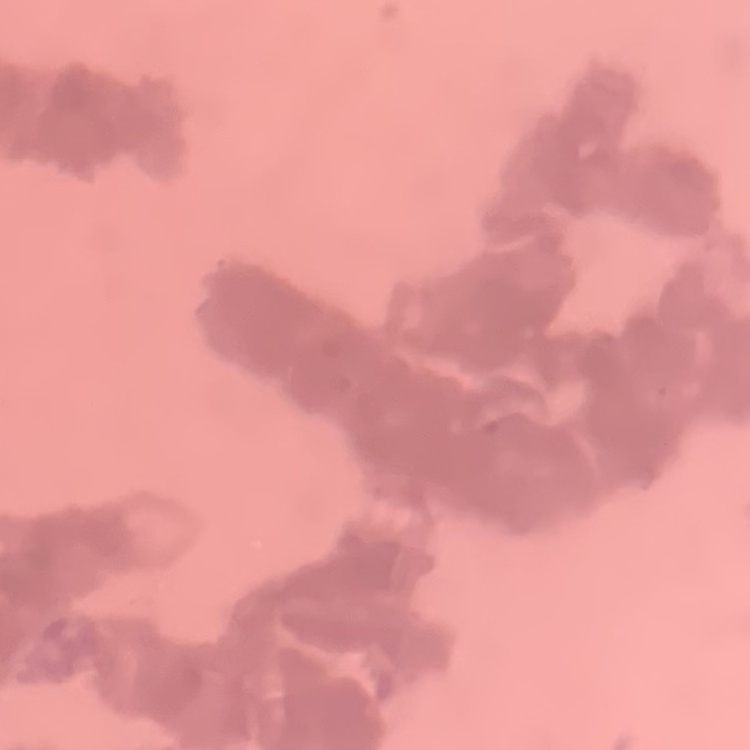

The erythrocytes exhibit rouleaux formation. Square crop of a larger photomicrograph. Thin peripheral smear. Stained with either Field's or Giemsa.